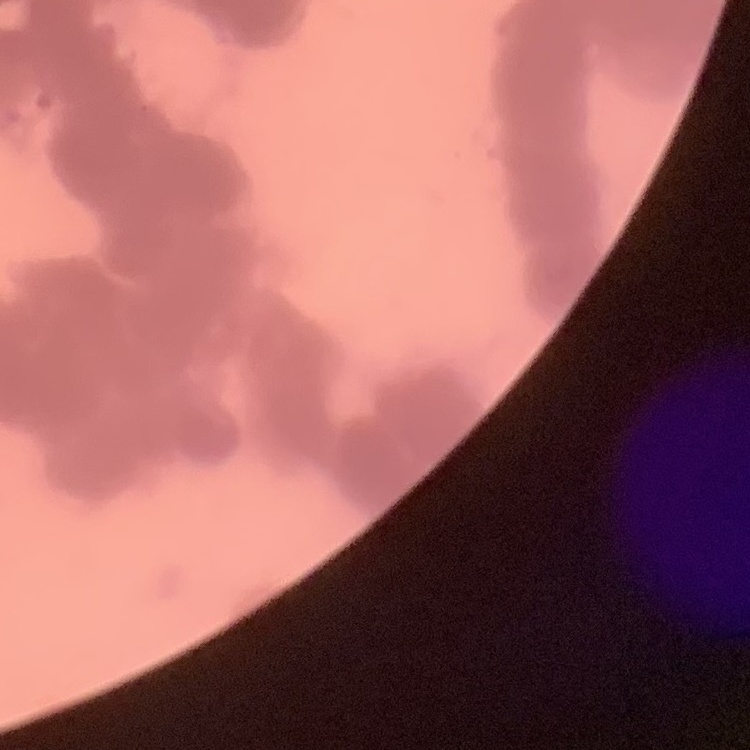

The erythrocytes exhibit rouleaux formation. Stained with either Field's or Giemsa. Thin blood film. One tile cut from a larger photomicrograph.